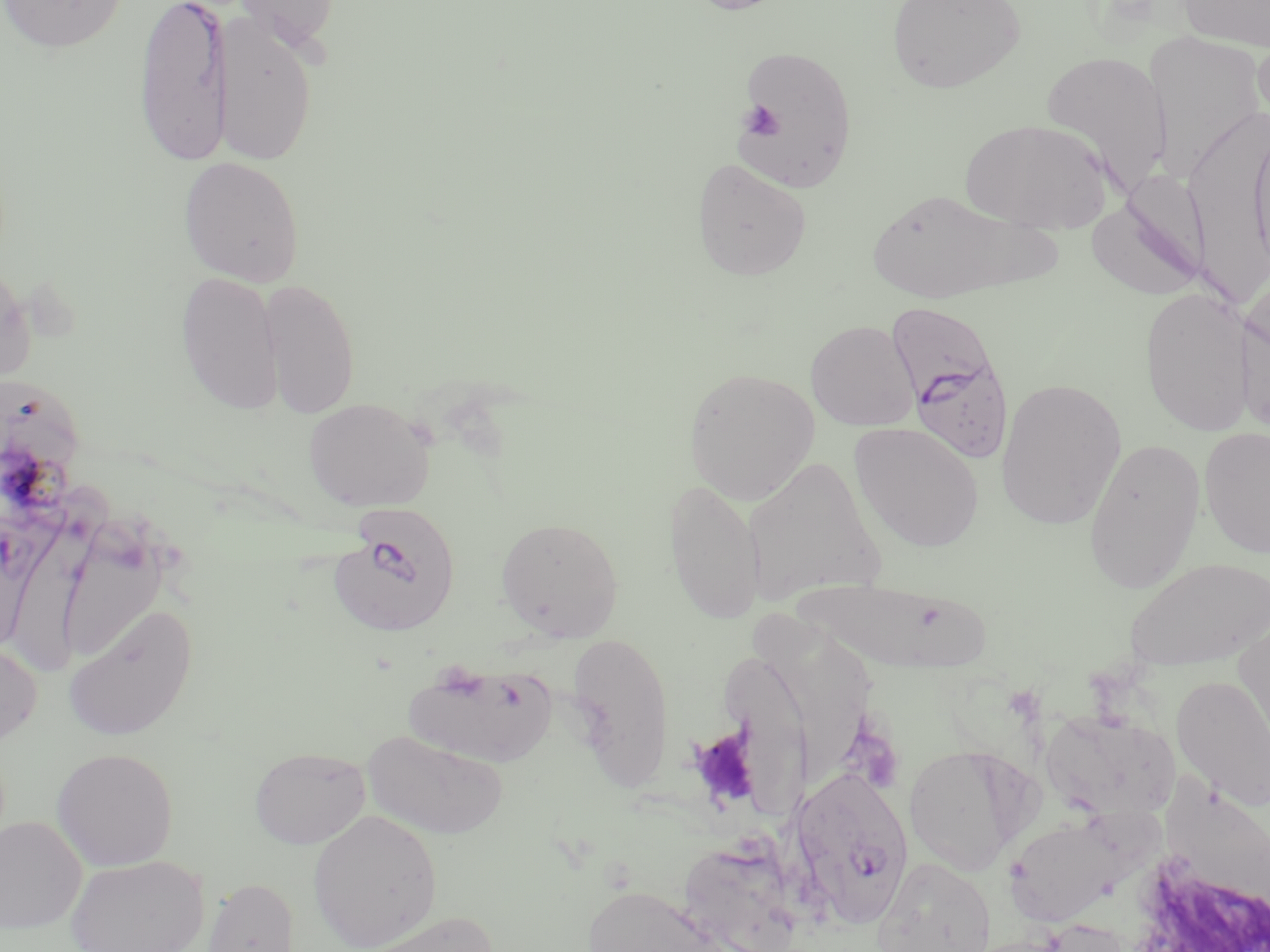
Approximate bounding boxes as (x1, y1, x2, y2) in pixels. Platelet locations: (741, 100, 784, 140), (686, 725, 764, 812). Plasmodium falciparum-infected red blood cell locations: (887, 299, 1019, 468), (328, 506, 462, 638), (790, 762, 916, 928). Uninfected red blood cell locations: (0, 0, 127, 54), (134, 0, 232, 166), (231, 0, 343, 55), (682, 0, 794, 15), (886, 0, 1025, 93), (1178, 0, 1270, 52), (214, 13, 319, 166), (1252, 29, 1270, 137), (1142, 30, 1267, 178), (732, 42, 858, 193), (1039, 49, 1174, 193), (1201, 106, 1268, 302), (960, 118, 1114, 234), (1247, 119, 1270, 278), (178, 156, 305, 286), (691, 157, 812, 280), (865, 187, 1033, 303), (1088, 192, 1209, 301), (0, 255, 35, 390), (176, 271, 283, 414), (259, 277, 361, 419), (1139, 286, 1258, 437), (1236, 289, 1270, 437), (806, 320, 920, 431), (683, 367, 820, 505), (995, 376, 1127, 530), (303, 397, 435, 511), (849, 422, 984, 552), (1199, 427, 1270, 559), (1082, 437, 1206, 593), (740, 454, 887, 608), (664, 477, 767, 625), (13, 479, 114, 669), (494, 517, 624, 641), (57, 527, 169, 664), (1122, 556, 1269, 670), (798, 574, 1001, 675), (64, 603, 198, 741), (1232, 607, 1270, 760), (747, 611, 882, 783), (567, 631, 674, 785), (723, 639, 819, 834), (0, 641, 41, 747), (404, 659, 558, 769), (1171, 675, 1270, 810), (1042, 709, 1180, 825), (362, 729, 510, 840), (904, 743, 1030, 875), (249, 746, 370, 848), (51, 747, 179, 870), (1157, 760, 1270, 923), (308, 809, 443, 950), (0, 815, 87, 933), (1004, 815, 1124, 927), (681, 840, 833, 952), (65, 854, 209, 952), (873, 855, 996, 952), (201, 877, 300, 952), (582, 883, 737, 952), (351, 910, 497, 952). Slide-level diagnosis: Plasmodium falciparum. Single field of view. Image is 1270×952 pixels. Thin blood smear. Captured at 1000x magnification. Optical microscopy. May-Grünwald-Giemsa-stained preparation.